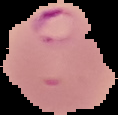 Cell region segmented out of the field of view; the surrounding area is masked to black. Image is 118×115 pixels. Result: malaria parasites identified. From a thin blood film.